Identify the preparation type.
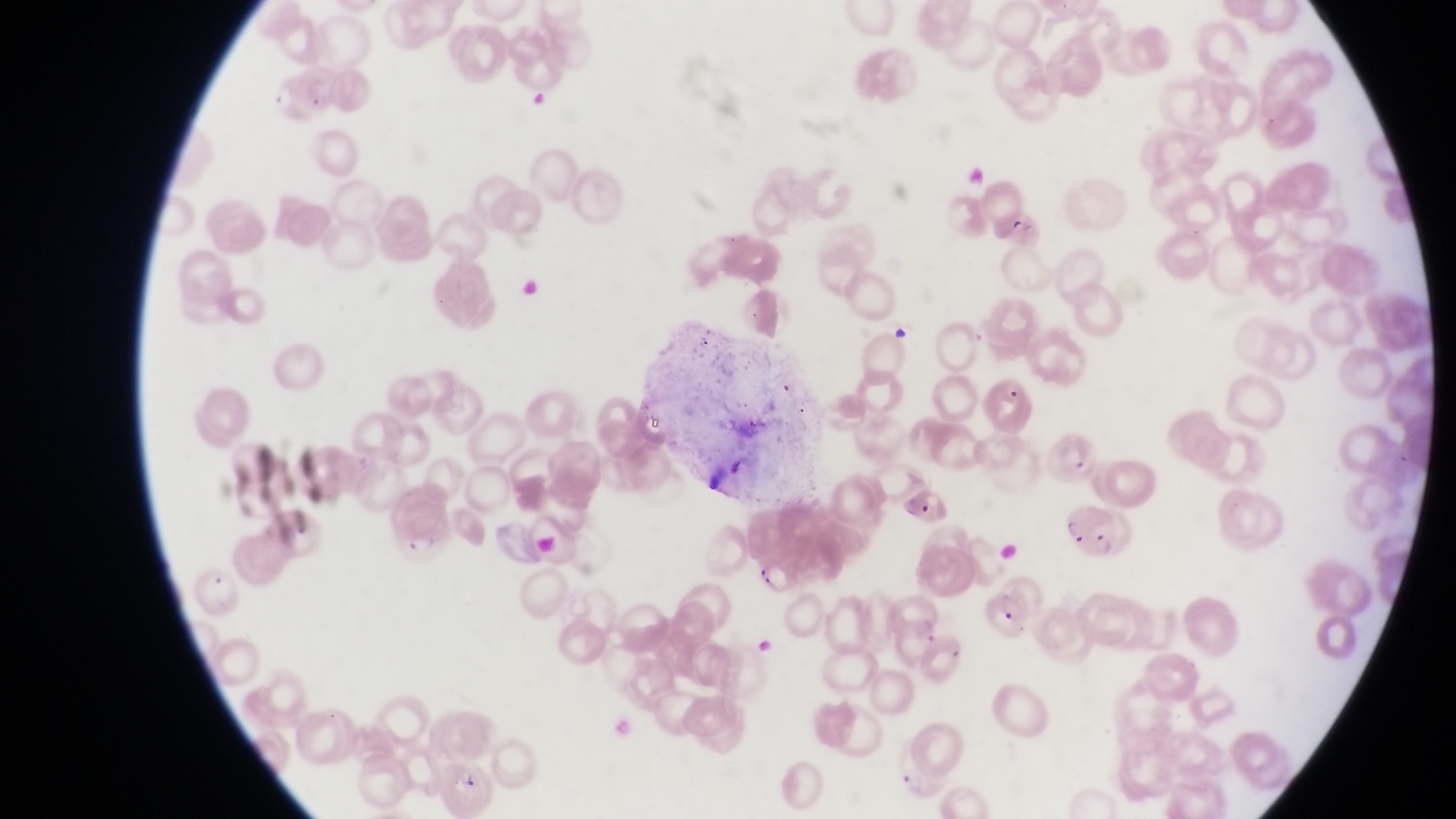

Thin blood smear.

magnification = 1000x
field of view = single
country = Uganda
capture = smartphone photograph through the eyepiece of an Olympus CX-23 microscope
parasitised red blood cell locations = approximate bounding boxes as left top right bottom in pixels: 986 376 1036 436; 1046 429 1098 479; 901 485 957 532; 1056 505 1128 554; 990 576 1053 650
image size = 1456×819 pixels
artifact (platelet-like body, stain precipitate, or debris) locations = approximate bounding boxes as left top right bottom in pixels: 529 86 548 107; 891 322 912 346